Identify the cell.
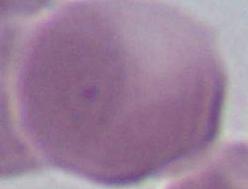
An erythrocyte.

modality = photomicrograph
magnification = 1000x